Report the malaria status of this cell.
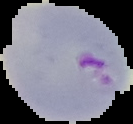
It is parasitized.

Summary:
  - Image size: 133×124 pixels
  - Preparation: thin blood film
  - Image type: cell region segmented out of the field of view; surrounding area masked to black